Assess this cell for malaria.
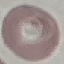

It is uninfected.

Acquired by smartphone through the microscope eyepiece. Giemsa-stained preparation. Thin blood smear. Automatically extracted cell patch, resized to 64 × 64 pixels.